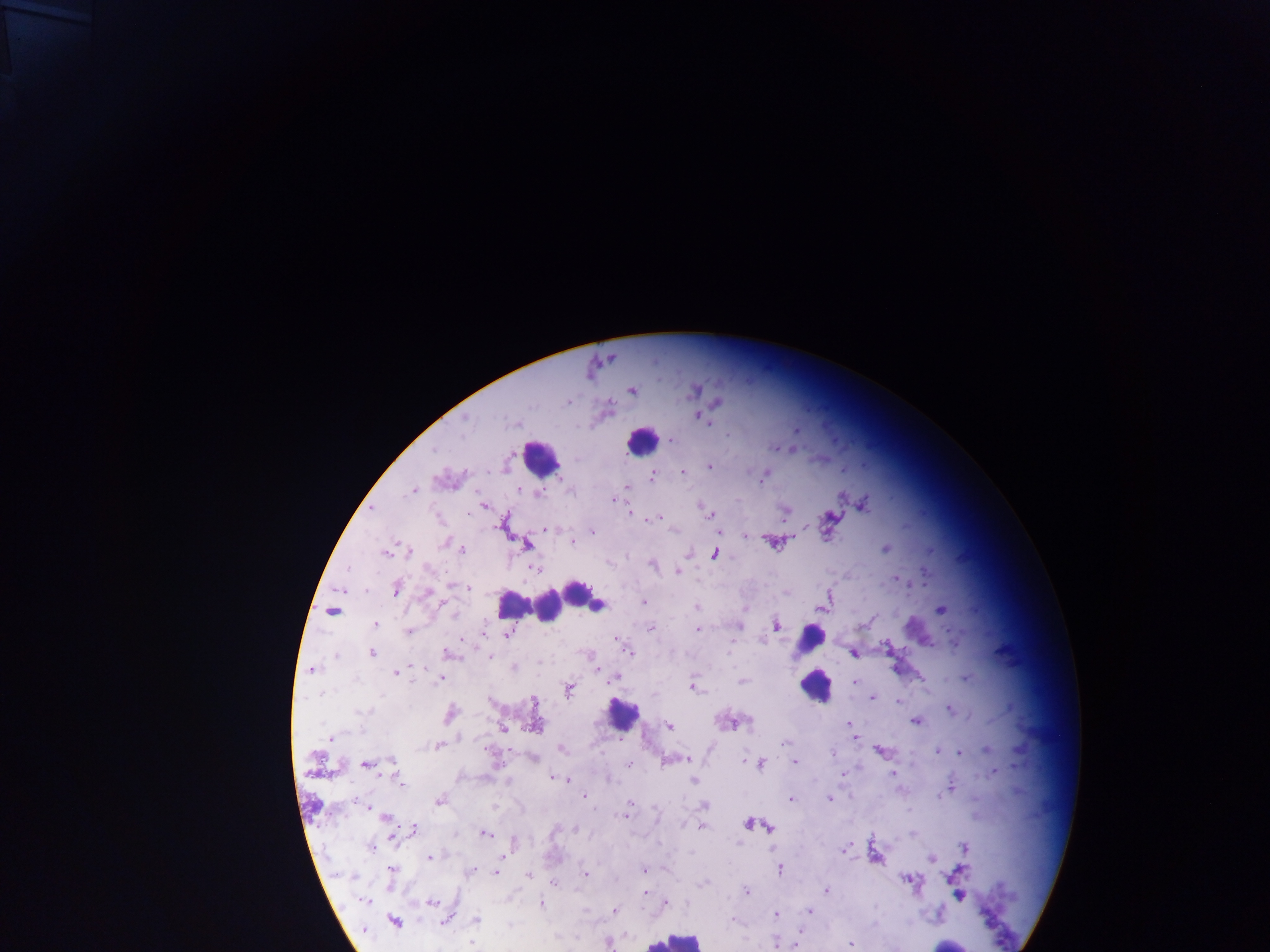
country: Ghana
malaria_parasite_locations: 'approximate centers as {x, y} in pixels: {631, 390}, {717, 402}, {567, 403}, {609, 405}, {699, 416}, {465, 419}, {709, 422}, {795, 429}, {728, 434}, {671, 440}, {775, 448}, {709, 466}, {683, 472}, {652, 476}, {762, 480}, {626, 486}, {519, 489}, {414, 490}, {614, 500}, {484, 505}, {863, 505}, {630, 513}, {711, 515}, {784, 515}, {660, 517}, {647, 520}, {546, 529}, {593, 532}, {718, 532}, {745, 536}, {572, 542}, {771, 542}, {444, 543}, {526, 544}, {886, 548}, {462, 549}, {409, 551}, {386, 553}, {687, 554}, {714, 554}, {652, 565}, {429, 568}, {534, 569}, {677, 571}, {896, 578}, {452, 586}, {467, 588}, {397, 589}, {428, 594}, {829, 596}, {644, 602}, {696, 607}, {820, 609}, {941, 610}, {332, 611}, {453, 613}, {376, 624}, {776, 625}, {738, 626}, {650, 628}, {698, 629}, {408, 631}, {507, 635}, {616, 640}, {955, 643}, {627, 649}, {371, 653}, {448, 654}, {854, 654}, {490, 655}, {335, 656}, {513, 668}, {598, 669}, {312, 670}, {396, 673}, {966, 678}, {439, 679}, {613, 679}, {742, 682}, {854, 682}, {568, 689}, {693, 689}, {872, 698}, {898, 701}, {534, 703}, {950, 709}, {362, 712}, {449, 714}, {915, 721}, {728, 723}, {848, 723}, {535, 726}, {669, 726}, {504, 728}, {332, 738}, {854, 738}, {784, 743}, {438, 745}, {560, 748}, {987, 748}, {937, 750}, {880, 751}, {832, 753}, {960, 753}, {533, 759}, {674, 760}, {686, 760}, {392, 761}, {795, 762}, {629, 763}, {366, 764}, {760, 764}, {994, 772}, {892, 774}, {555, 778}, {608, 778}, {694, 780}, {400, 782}, {950, 787}, {584, 796}, {830, 799}, {438, 800}, {790, 800}, {630, 802}, {703, 806}, {626, 809}, {623, 816}, {384, 817}, {747, 823}, {701, 826}, {768, 827}, {575, 828}, {415, 829}, {484, 833}, {913, 834}, {964, 847}, {371, 848}, {844, 850}, {430, 857}, {505, 857}, {931, 858}, {644, 870}, {779, 870}, {471, 871}, {961, 871}, {392, 872}, {497, 873}, {528, 874}, {585, 874}, {908, 880}, {553, 883}, {703, 883}, {826, 890}, {747, 891}, {646, 892}, {958, 895}, {364, 900}, {432, 903}, {542, 904}, {665, 904}, {614, 910}, {808, 911}, {776, 914}, {732, 919}, {477, 920}, {446, 921}, {395, 922}, {608, 942}, {775, 942}, {472, 943}, {851, 944}'
preparation: thick blood smear
image_size: 1270×952 pixels
leukocyte_locations: 'approximate centers as {x, y} in pixels: {642, 440}, {541, 458}, {578, 592}, {594, 602}, {515, 606}, {549, 606}, {810, 639}, {814, 686}, {622, 714}, {674, 940}, {944, 945}'
field_of_view: single
capture: mobile-phone photograph through a microscope